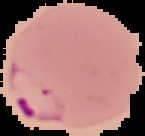

Image is 145×136 pixels. From a thin blood smear. Malaria status: parasitized. Segmented cell region on a black background.